Identify the parasite.
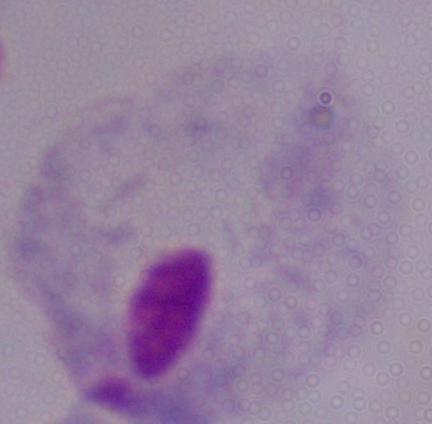
A trichomonad.

Captured at 1000x magnification. Photomicrograph.